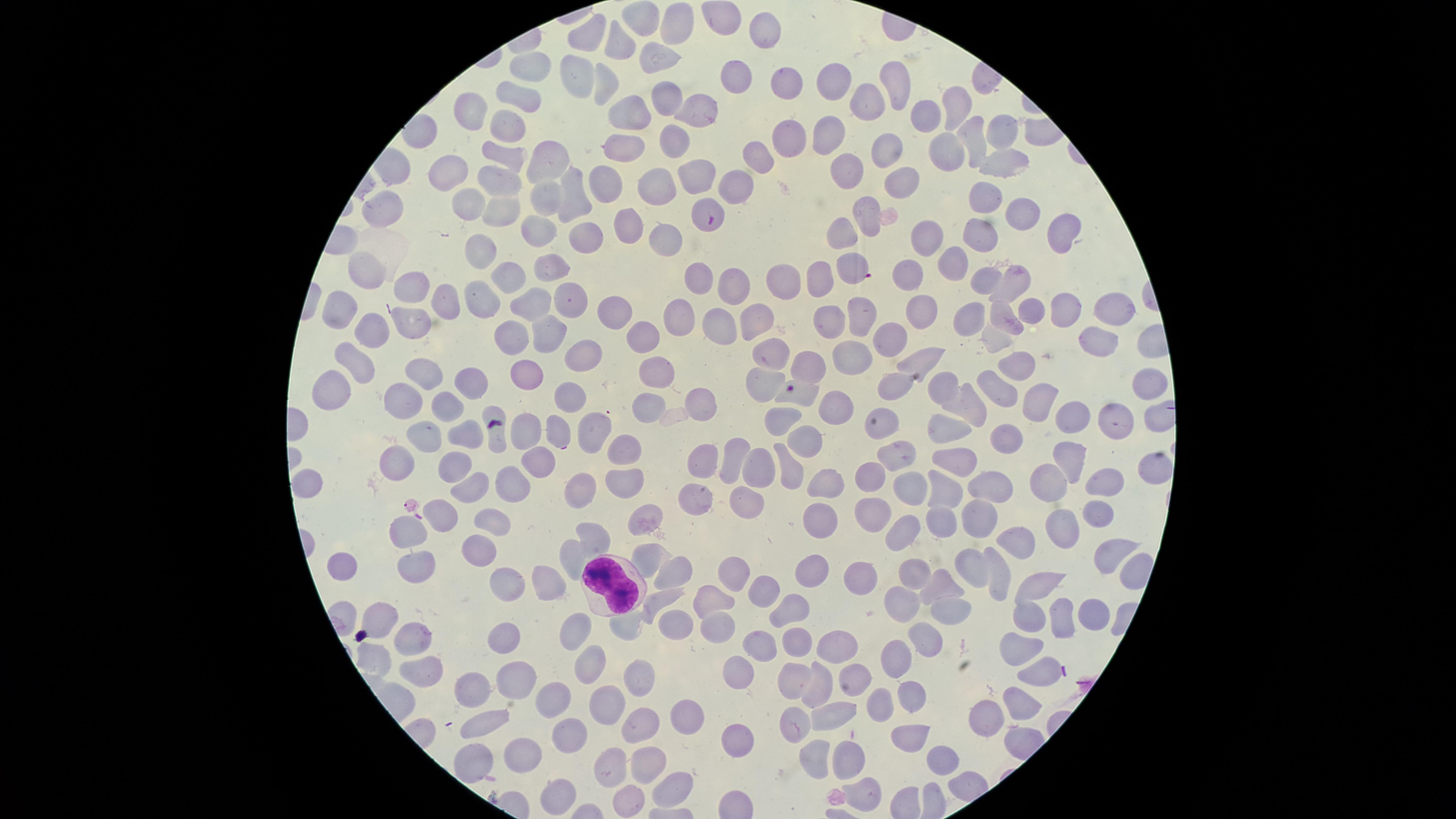

Approximate marker points as {x, y} in pixels.
Summary:
  - White blood cells: {609, 582}
  - Parasitized red blood cells: {713, 220}, {856, 271}, {797, 391}
  - Uninfected red blood cells: {640, 17}, {719, 18}, {674, 25}, {766, 26}, {584, 27}, {617, 46}, {651, 58}, {530, 70}, {576, 71}, {738, 74}, {896, 79}, {785, 80}, {601, 81}, {831, 84}, {522, 96}, {662, 101}, {860, 102}, {958, 102}, {472, 107}, {692, 114}, {924, 114}, {624, 116}, {511, 119}, {827, 133}, {977, 134}, {1000, 135}, {670, 138}, {790, 140}, {884, 146}, {950, 149}, {505, 152}, {758, 154}, {541, 163}, {1003, 169}, {449, 171}, {844, 173}, {693, 176}, {899, 178}, {735, 179}, {662, 180}, {497, 183}, {597, 183}, {574, 190}, {982, 192}, {387, 202}, {464, 206}, {548, 206}, {866, 208}, {1020, 211}, {494, 214}, {622, 227}, {536, 228}, {926, 229}, {1063, 229}, {842, 232}, {987, 232}, {580, 236}, {669, 237}, {486, 251}, {948, 259}, {552, 264}, {362, 265}, {785, 272}, {907, 272}, {985, 275}, {701, 276}, {508, 277}, {816, 278}, {731, 282}, {1013, 283}, {415, 289}, {483, 295}, {448, 297}, {569, 300}, {524, 305}, {1059, 305}, {343, 306}, {918, 307}, {1031, 307}, {1104, 309}, {1001, 310}, {965, 312}, {856, 315}, {681, 316}, {607, 317}, {751, 320}, {833, 320}, {722, 321}, {376, 329}, {556, 333}, {642, 333}, {511, 338}, {891, 338}, {993, 339}, {1096, 341}, {772, 350}, {848, 352}, {580, 353}, {921, 356}, {1020, 361}, {355, 364}, {658, 365}, {807, 369}, {526, 370}, {421, 373}, {470, 382}, {761, 382}, {334, 384}, {890, 384}, {944, 386}, {1149, 386}, {994, 387}, {571, 392}, {1041, 394}, {404, 397}, {698, 402}, {447, 405}, {967, 406}, {646, 408}, {833, 409}, {1069, 411}, {783, 415}, {1112, 417}, {946, 423}, {525, 425}, {590, 426}, {553, 429}, {464, 431}, {421, 434}, {1007, 434}, {495, 435}, {810, 440}, {623, 450}, {899, 453}, {1075, 456}, {956, 457}, {702, 459}, {734, 459}, {537, 462}, {398, 463}, {757, 466}, {453, 467}, {1154, 467}, {790, 475}, {1052, 477}, {870, 478}, {622, 479}, {512, 480}, {1106, 480}, {474, 482}, {304, 483}, {574, 483}, {832, 483}, {993, 486}, {908, 488}, {942, 489}, {693, 496}, {747, 500}, {1097, 511}, {438, 512}, {647, 514}, {876, 514}, {492, 518}, {948, 520}, {978, 520}, {817, 524}, {1064, 527}, {588, 529}, {904, 530}, {406, 533}, {1014, 544}, {568, 547}, {480, 549}, {646, 556}, {1111, 557}, {337, 563}, {411, 567}, {970, 567}, {995, 567}, {805, 569}, {910, 571}, {732, 573}, {547, 574}, {669, 574}, {859, 579}, {1041, 583}, {942, 585}, {505, 591}, {760, 591}, {711, 600}, {661, 602}, {897, 602}, {790, 605}, {946, 607}, {1064, 611}, {1026, 614}, {1091, 614}, {381, 620}, {633, 624}, {674, 624}, {720, 628}, {571, 634}, {507, 636}, {763, 637}, {923, 637}, {409, 639}, {798, 639}, {838, 645}, {1017, 649}, {373, 655}, {590, 659}, {893, 661}, {419, 666}, {1039, 668}, {734, 675}, {848, 676}, {795, 681}, {514, 682}, {820, 682}, {639, 683}, {476, 691}, {909, 694}, {556, 695}, {1013, 702}, {609, 705}, {836, 707}, {880, 707}, {796, 717}, {981, 718}, {497, 720}, {683, 720}, {641, 729}, {567, 730}, {903, 733}, {735, 739}, {523, 752}, {813, 752}, {470, 755}, {943, 756}, {617, 759}, {647, 759}, {849, 759}, {671, 782}, {552, 786}, {864, 788}, {625, 790}
  - Stain: Giemsa
  - Visible region: circular
  - Capture: smartphone photograph through the microscope eyepiece
  - Species: Plasmodium falciparum
  - Presence: malaria parasites seen
  - Preparation: thin smear of blood
  - Field of view: single
  - Image size: 1456×819 pixels